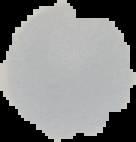
image size = 136×142 pixels
preparation = thin blood film
malaria status = uninfected
image type = segmented cell region on a black background